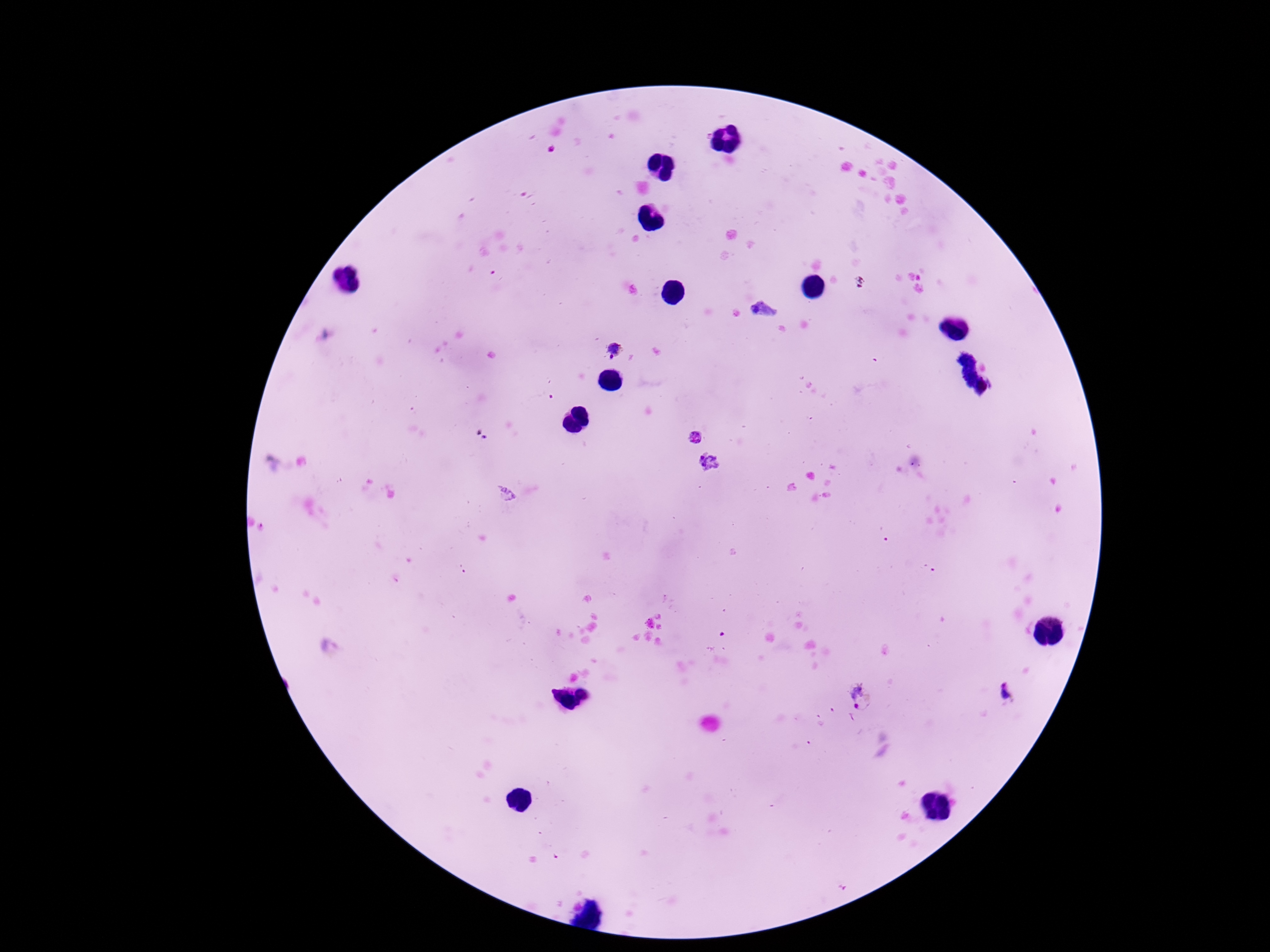
Approximate centers as {x, y} in pixels.
Summary:
  - Plasmodium parasite locations: {615, 350}, {695, 436}, {708, 463}, {1008, 692}, {863, 698}
  - Capture: smartphone camera through the microscope eyepiece
  - Image size: 1270×952 pixels
  - Patient malaria status: positive
  - Preparation: thick blood film
  - Stain: Giemsa
  - Magnification: 100x
  - Field of view: one from this slide